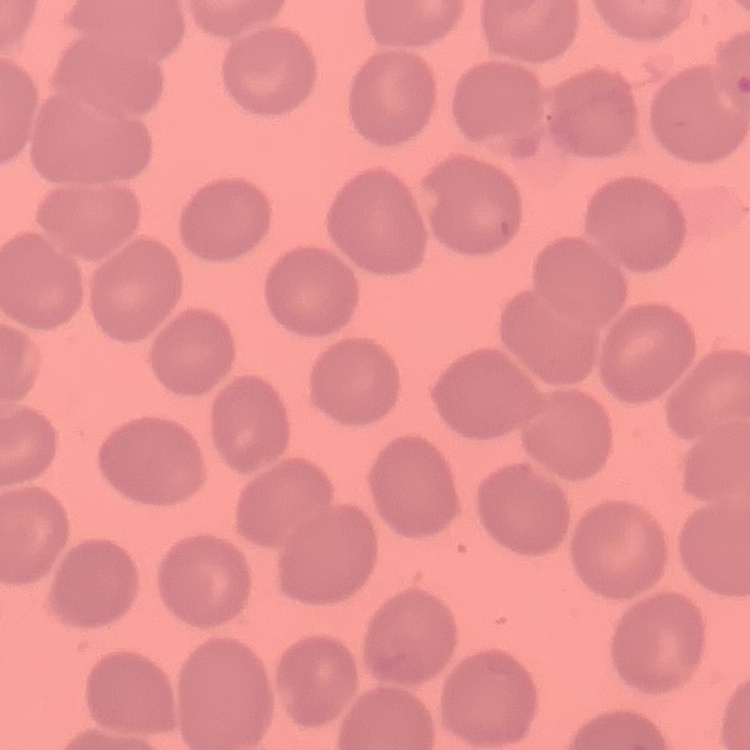
Summary:
  - Red blood cell morphology: no rouleaux formation
  - Preparation: thin blood film
  - Image type: one tile cut from a larger photomicrograph
  - Stain: Field's or Giemsa